Give the extent of all Plasmodium vivax-infected red blood cells.
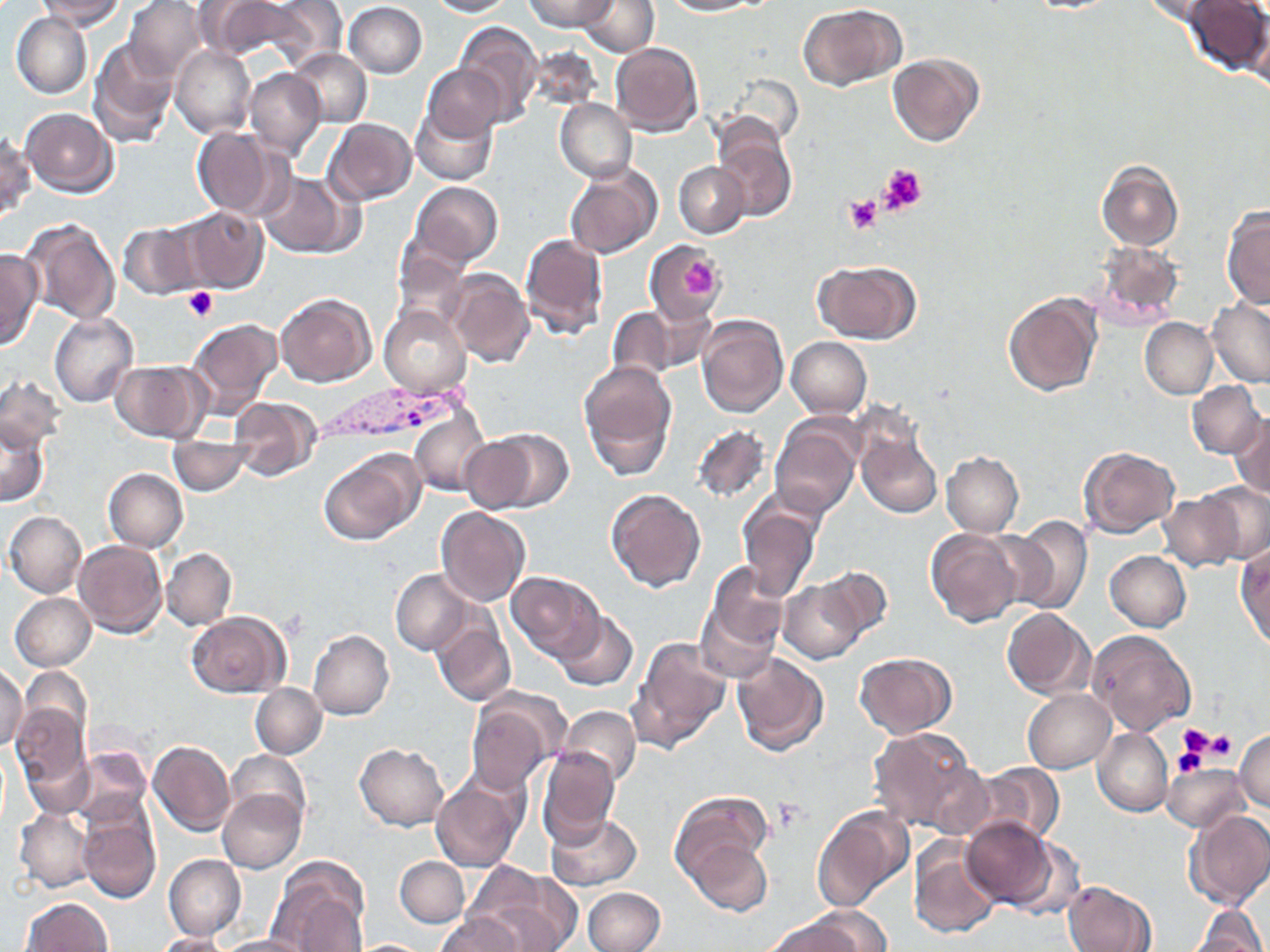
Approximate bounding boxes as (x1,y1)-(x2,y2) corner pairs in pixels.
Plasmodium vivax-infected red blood cells: (325,387)-(470,438).

slide_level_diagnosis: Plasmodium vivax
image_size: 1270×952 pixels
magnification: 1000x
field_of_view: one of a larger specimen
modality: light microscopy
uninfected_red_blood_cell_locations: 'approximate bounding boxes as (x1,y1)-(x2,y2) corner pairs in pixels: (125,0)-(207,81), (425,0)-(516,16), (524,0)-(616,31), (666,0)-(765,16), (1186,0)-(1269,76), (39,1)-(126,31), (205,1)-(326,65), (344,1)-(428,78), (1140,1)-(1234,31), (576,2)-(659,58), (796,3)-(908,93), (11,15)-(90,97), (454,20)-(540,127), (89,39)-(178,147), (612,42)-(704,136), (535,44)-(602,113), (171,45)-(256,138), (290,49)-(371,125), (888,53)-(985,147), (424,65)-(505,141), (245,69)-(324,160), (554,98)-(635,181), (412,105)-(496,185), (21,108)-(116,198), (326,118)-(417,205), (192,127)-(286,220), (713,128)-(799,223), (1,129)-(34,221), (1098,160)-(1184,250), (674,162)-(748,237), (566,167)-(660,259), (258,172)-(349,257), (409,181)-(503,268), (1222,205)-(1270,309), (183,206)-(267,293), (23,218)-(120,325), (119,221)-(201,301), (520,232)-(609,340), (393,240)-(473,332), (1095,244)-(1184,329), (647,245)-(724,318), (0,249)-(43,350), (812,260)-(920,344), (445,268)-(533,366), (275,292)-(376,386), (1002,292)-(1102,397), (1206,297)-(1270,385), (642,302)-(718,375), (379,306)-(471,398), (607,306)-(681,388), (50,312)-(139,407), (696,315)-(788,417), (187,317)-(284,419), (1139,317)-(1218,399), (787,337)-(873,419), (110,360)-(210,443), (580,361)-(677,480), (1,374)-(64,455), (1186,380)-(1266,459), (229,398)-(323,479), (410,409)-(494,494), (1230,411)-(1269,500), (0,416)-(49,507), (771,419)-(863,522), (690,425)-(771,506), (485,428)-(573,512), (856,429)-(942,520), (461,436)-(538,513), (171,437)-(252,493), (1079,446)-(1180,538), (318,448)-(423,545), (942,451)-(1023,535), (104,468)-(187,551), (1199,479)-(1270,566), (606,489)-(708,592), (1158,490)-(1247,572), (740,499)-(821,603), (437,507)-(530,608), (4,511)-(86,597), (1010,516)-(1093,615), (927,529)-(1024,628), (73,540)-(168,637), (1236,545)-(1269,651), (163,548)-(236,629), (1105,550)-(1191,632), (697,564)-(789,679), (813,566)-(892,649), (391,570)-(470,655), (508,570)-(602,660), (779,578)-(867,664), (9,590)-(96,671), (1002,608)-(1095,699), (186,611)-(289,697), (555,611)-(636,692), (433,618)-(515,706), (308,630)-(394,719), (1088,630)-(1197,735), (631,638)-(731,750), (854,651)-(957,739), (733,653)-(829,757), (0,661)-(27,753), (22,667)-(89,735), (250,684)-(327,757), (1023,688)-(1116,772), (11,695)-(90,800), (467,699)-(560,794), (560,706)-(641,785), (866,726)-(983,837), (1093,729)-(1173,816), (1233,729)-(1270,810), (147,739)-(235,835), (355,743)-(449,830), (537,747)-(620,843), (229,751)-(310,829), (72,752)-(151,831), (970,761)-(1066,845), (1165,761)-(1251,830), (431,772)-(527,872), (217,790)-(303,873), (669,791)-(777,900), (76,801)-(161,904), (811,804)-(914,912), (13,805)-(96,895), (1185,808)-(1270,910), (544,811)-(644,890), (963,815)-(1059,907), (684,834)-(775,916), (907,841)-(1000,939), (163,853)-(245,941), (395,856)-(469,928), (268,858)-(369,952), (466,863)-(581,951), (1065,879)-(1156,952), (583,886)-(667,952), (21,897)-(114,951), (1190,902)-(1267,952), (434,913)-(525,952), (762,915)-(876,952), (153,933)-(228,952), (214,934)-(313,952)'
platelet_locations: 'approximate bounding boxes as (x1,y1)-(x2,y2) corner pairs in pixels: (879,163)-(925,212), (843,195)-(882,233), (683,260)-(716,295), (182,286)-(220,322), (1176,722)-(1217,760), (1199,728)-(1239,763), (1173,742)-(1209,778), (769,796)-(808,833)'
preparation: thin blood smear
stain: May-Grünwald-Giemsa